Assess this cell for malaria.
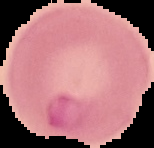

It is parasitized.

{
  "image_type": "segmented cell region on a black background",
  "preparation": "thin blood film",
  "image_size": "154×148 pixels"
}